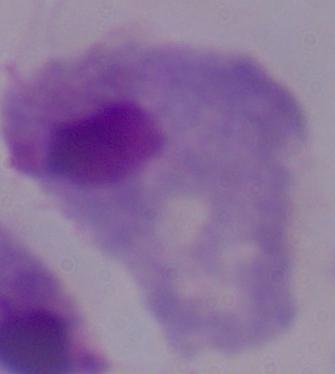

Micrograph. A trichomonad is seen. 1000x magnification.